Assess this cell for malaria.
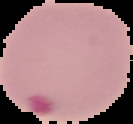
It is parasitized.

Image is 133×124 pixels. From a thin blood film. The area outside the segmented cell region is set to black.